Locate Plasmodium parasites and leukocytes.
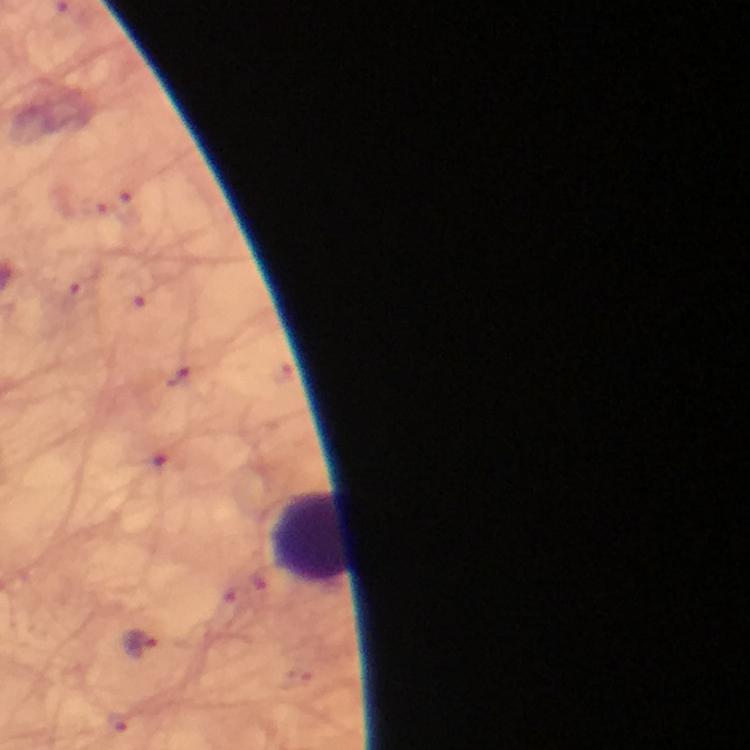

Approximate object centers, in pixels from the top-left corner.
Plasmodium parasites: (x=142, y=644).
Leukocytes: (x=312, y=539).

image size = 750×750 pixels
context = from a malaria diagnostic workup
capture = smartphone camera through the microscope
immersion oil = applied
stain = Giemsa
preparation = thick smear
magnification = 100x
cropped from = one field of view